Name the cell type shown.
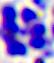
This is a leukocyte.

Summary:
  - Magnification: 400x
  - Modality: photomicrograph